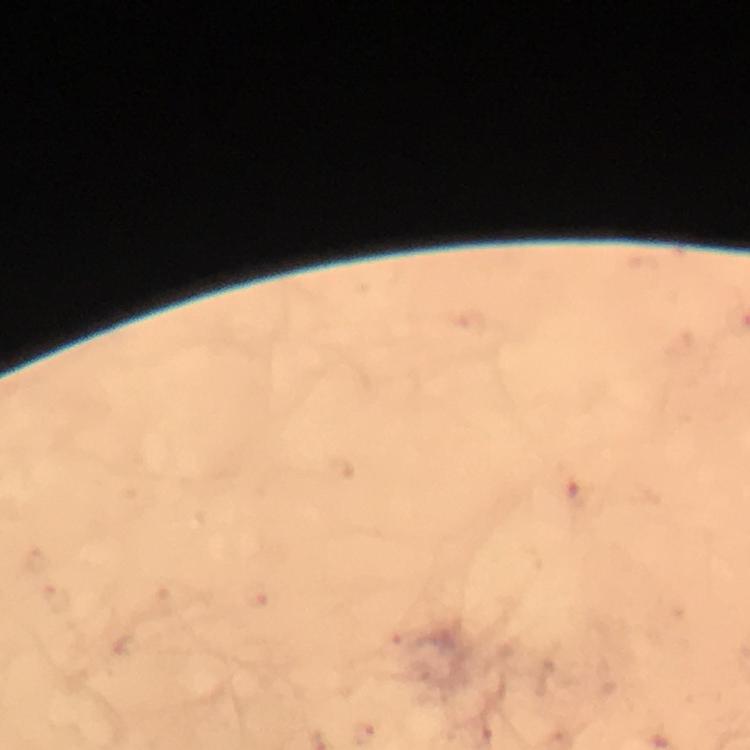
Approximate object centers, in pixels from the top-left corner. Malaria parasite locations: (x=578, y=495), (x=362, y=733). Thick blood smear. Image is 750×750 pixels. Giemsa stain. 100x magnification. Smartphone photograph taken through a microscope. A crop from one field of view. Immersion oil applied. From a malaria diagnostic workup.